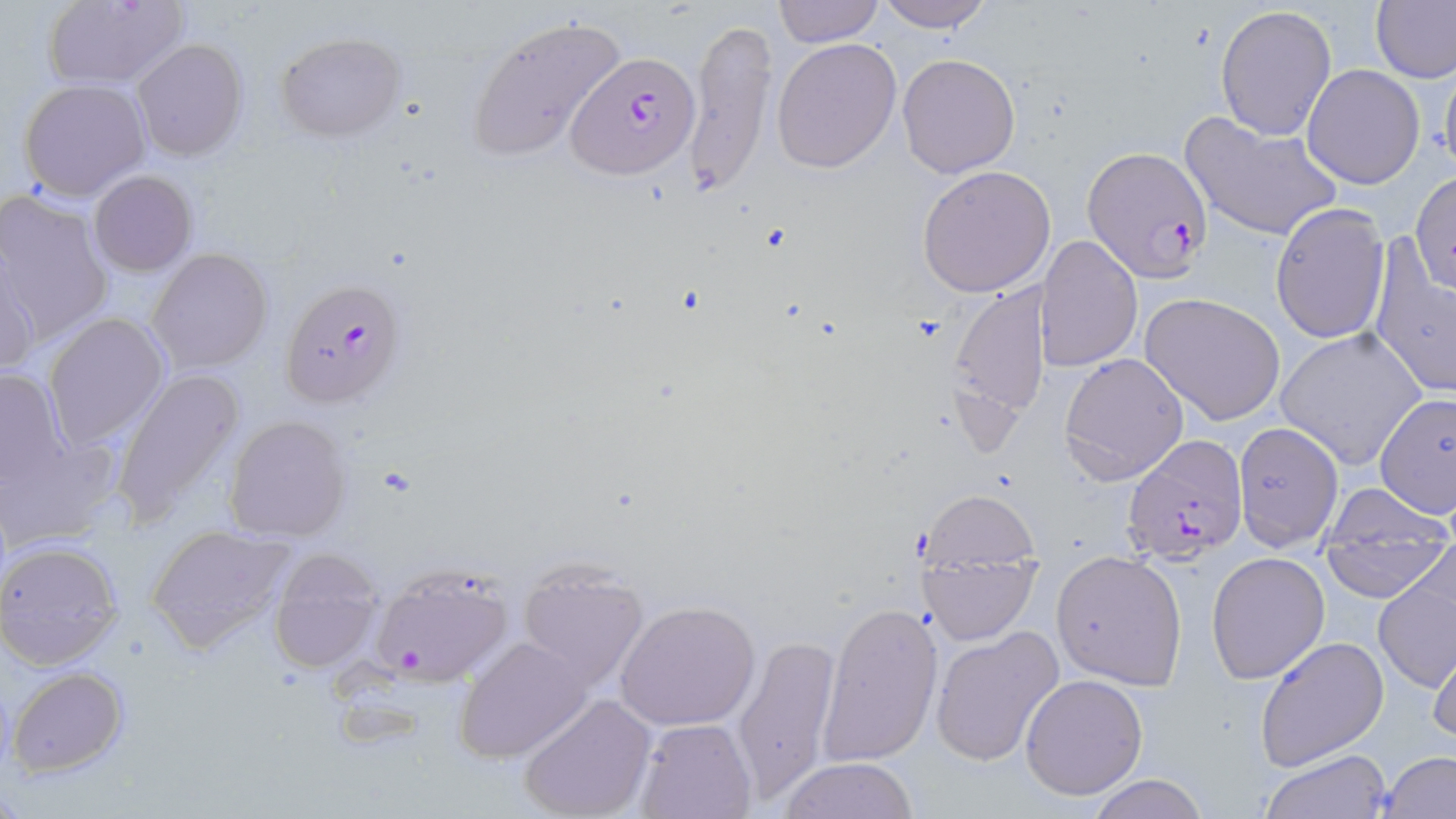 Approximate bounding boxes as (x1, y1, x2, y2) in pixels. Plasmodium falciparum-infected red blood cell locations: (568, 50, 700, 178), (1087, 145, 1215, 282), (282, 278, 407, 408), (1121, 433, 1247, 563), (367, 557, 519, 685). Uninfected red blood cell locations: (42, 0, 189, 90), (772, 0, 884, 48), (875, 0, 994, 31), (1372, 0, 1455, 84), (1215, 5, 1337, 141), (466, 13, 629, 163), (684, 18, 778, 197), (275, 32, 406, 140), (772, 38, 902, 174), (131, 39, 248, 160), (897, 52, 1021, 178), (1438, 54, 1456, 187), (1301, 64, 1425, 188), (19, 79, 150, 200), (1180, 111, 1343, 243), (917, 165, 1053, 297), (89, 170, 197, 276), (1413, 172, 1455, 297), (0, 191, 113, 341), (1269, 202, 1390, 343), (1039, 236, 1143, 373), (1368, 241, 1455, 399), (147, 247, 273, 373), (0, 253, 41, 377), (1320, 267, 1433, 442), (946, 277, 1051, 427), (1138, 292, 1287, 426), (42, 311, 170, 451), (1277, 327, 1427, 468), (1059, 351, 1188, 486), (1, 366, 71, 492), (112, 367, 245, 523), (1375, 392, 1454, 522), (224, 415, 352, 543), (1232, 423, 1345, 554), (2, 431, 119, 550), (1322, 481, 1451, 561), (919, 490, 1040, 581), (145, 523, 298, 653), (1323, 525, 1447, 598), (0, 538, 123, 669), (267, 547, 385, 674), (1050, 549, 1188, 689), (1206, 550, 1331, 684), (918, 551, 1038, 645), (1374, 559, 1455, 696), (517, 560, 649, 690), (613, 599, 761, 732), (817, 599, 944, 766), (930, 625, 1064, 765), (731, 633, 840, 803), (455, 636, 594, 763), (1255, 636, 1389, 772), (1427, 637, 1456, 750), (8, 667, 127, 776), (1020, 673, 1149, 800), (517, 694, 654, 819), (635, 717, 756, 819), (1260, 748, 1391, 818), (1378, 750, 1455, 819), (778, 757, 921, 817), (1086, 775, 1211, 819). Slide-level diagnosis: Plasmodium falciparum. 1000x magnification. Light microscopy. Thin blood film. Image is 1456×819 pixels. One field of a larger specimen. May-Grünwald-Giemsa-stained preparation.